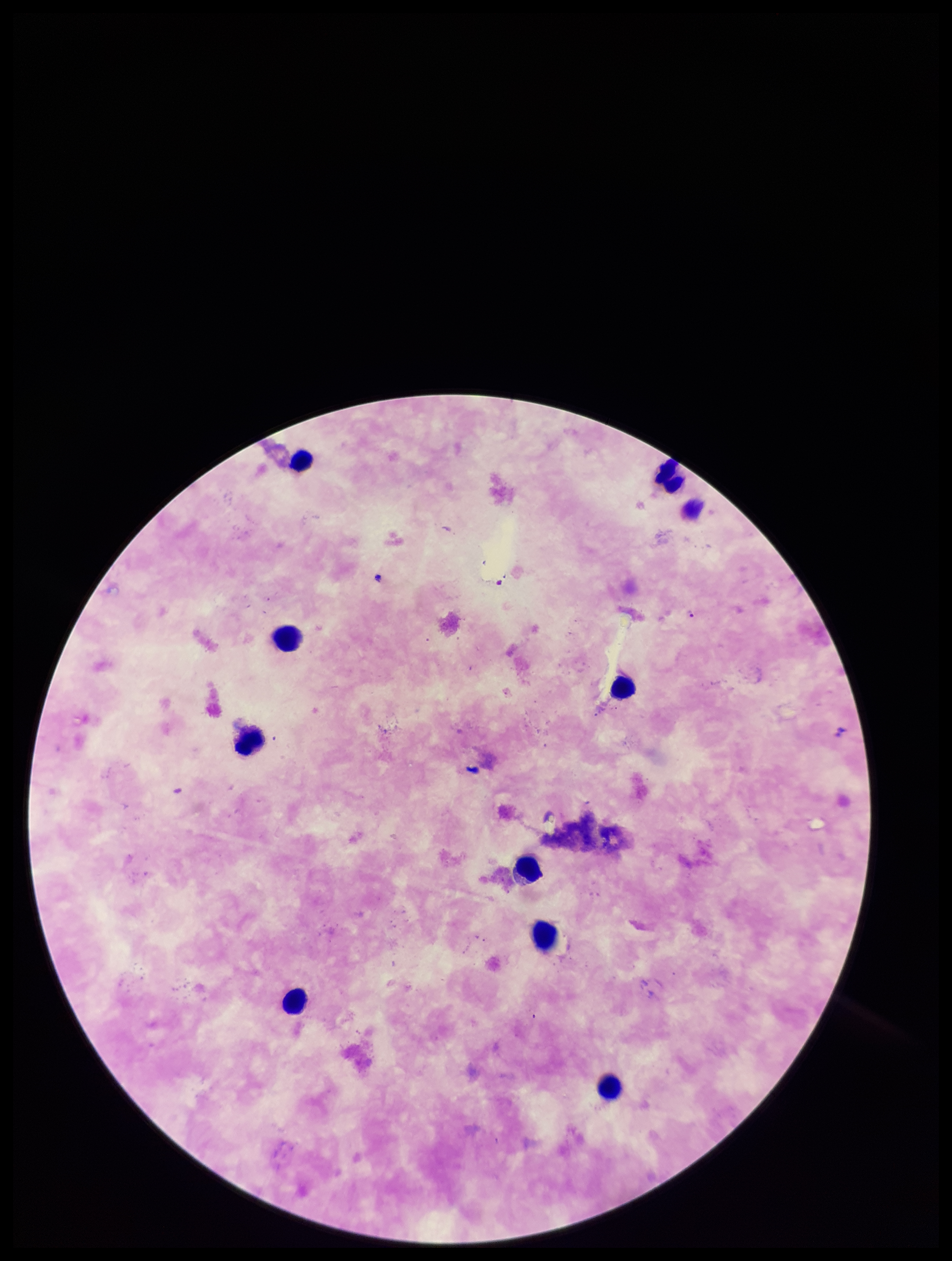

Summary:
  - Image size: 952×1261 pixels
  - Species reported for this patient: Plasmodium falciparum
  - Plasmodium parasites: identified
  - Stain: Giemsa
  - Leukocyte count: 10
  - Parasite count: 1
  - Field of view: one from this slide
  - Patient malaria status: infected
  - Capture: smartphone photograph through the microscope eyepiece
  - Preparation: thick smear